Locate every Plasmodium parasite.
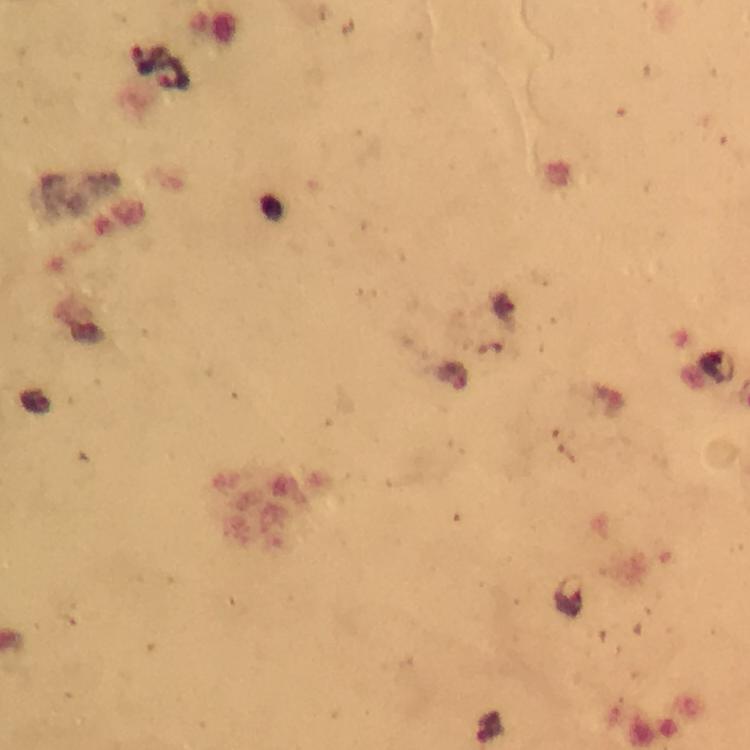
Approximate centers as (x, y) in pixels.
Plasmodium parasites: (148, 59), (175, 74), (568, 598), (489, 729).

Thick blood smear. Immersion oil applied. Giemsa stain. 100x magnification. Image is 750×750 pixels. From a malaria diagnostic workup. Photographed with a smartphone mounted on the microscope. A crop from one field of view.